Give the extent of all Plasmodium vivax-infected red blood cells.
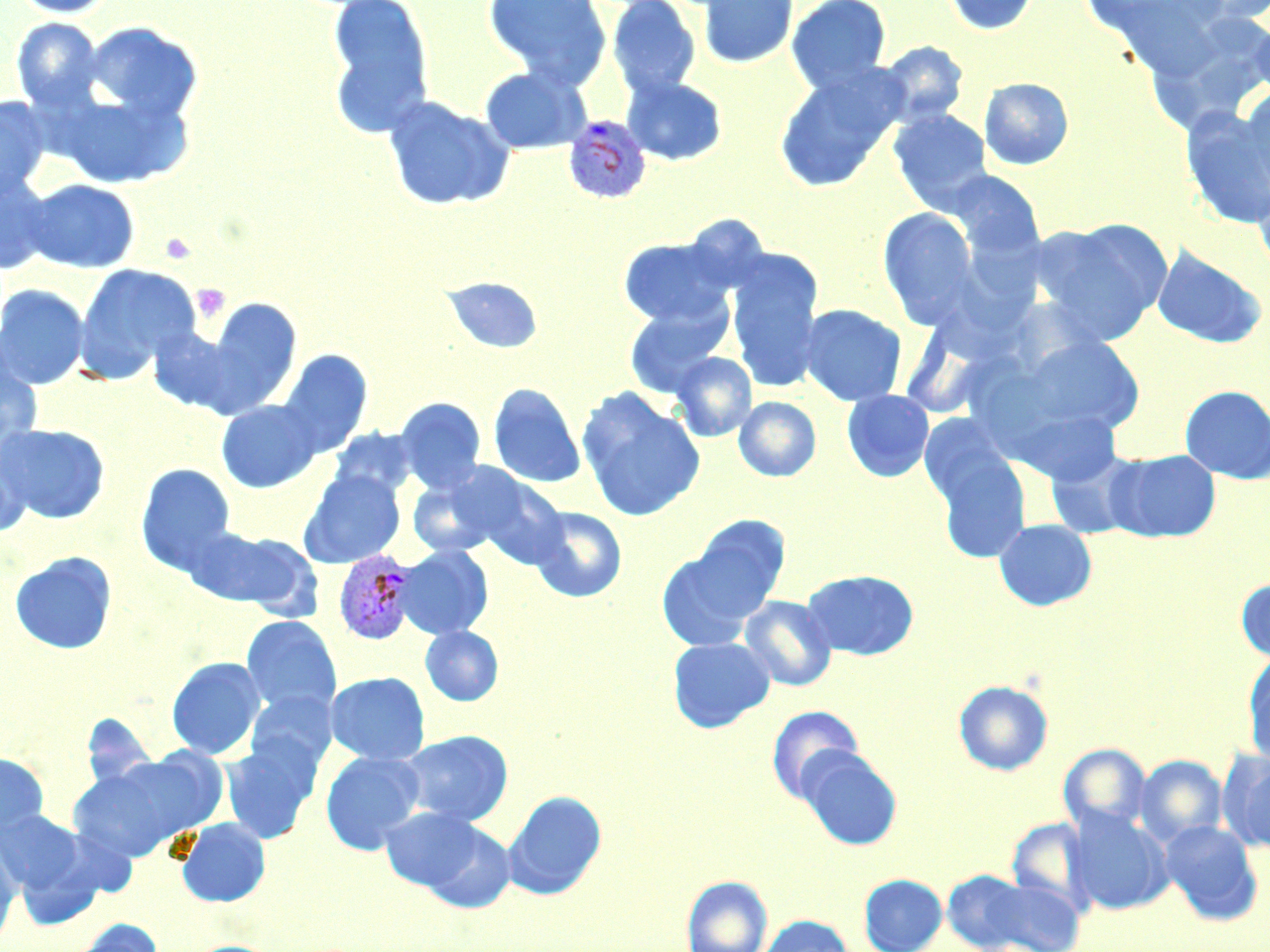
Approximate bounding boxes as named x1/y1/x2/y2 corners in pixels.
Plasmodium vivax-infected red blood cells: (x1=563, y1=115, x2=652, y2=203), (x1=334, y1=550, x2=418, y2=645).

Summary:
  - Uninfected red blood cell locations: (x1=9, y1=0, x2=118, y2=18), (x1=326, y1=0, x2=436, y2=137), (x1=483, y1=0, x2=611, y2=88), (x1=607, y1=0, x2=701, y2=100), (x1=697, y1=0, x2=798, y2=69), (x1=786, y1=0, x2=891, y2=94), (x1=939, y1=0, x2=1040, y2=36), (x1=1188, y1=0, x2=1270, y2=26), (x1=1249, y1=15, x2=1270, y2=100), (x1=11, y1=17, x2=105, y2=112), (x1=83, y1=21, x2=203, y2=122), (x1=878, y1=41, x2=968, y2=128), (x1=774, y1=66, x2=907, y2=192), (x1=480, y1=67, x2=587, y2=154), (x1=622, y1=76, x2=728, y2=166), (x1=979, y1=77, x2=1074, y2=170), (x1=1236, y1=86, x2=1270, y2=197), (x1=51, y1=88, x2=193, y2=189), (x1=0, y1=96, x2=51, y2=200), (x1=383, y1=96, x2=515, y2=211), (x1=1181, y1=108, x2=1270, y2=228), (x1=889, y1=109, x2=992, y2=214), (x1=947, y1=169, x2=1045, y2=262), (x1=0, y1=171, x2=55, y2=274), (x1=23, y1=178, x2=139, y2=273), (x1=1253, y1=178, x2=1270, y2=279), (x1=878, y1=208, x2=979, y2=327), (x1=1031, y1=220, x2=1172, y2=344), (x1=618, y1=237, x2=733, y2=328), (x1=1151, y1=245, x2=1268, y2=349), (x1=726, y1=250, x2=825, y2=393), (x1=73, y1=263, x2=199, y2=382), (x1=443, y1=276, x2=544, y2=354), (x1=0, y1=284, x2=90, y2=389), (x1=201, y1=297, x2=302, y2=410), (x1=623, y1=301, x2=731, y2=399), (x1=799, y1=304, x2=907, y2=406), (x1=146, y1=326, x2=242, y2=414), (x1=1020, y1=335, x2=1145, y2=436), (x1=0, y1=344, x2=44, y2=458), (x1=278, y1=350, x2=373, y2=457), (x1=671, y1=352, x2=757, y2=441), (x1=488, y1=383, x2=586, y2=488), (x1=1179, y1=385, x2=1270, y2=484), (x1=577, y1=389, x2=706, y2=521), (x1=842, y1=390, x2=934, y2=482), (x1=734, y1=396, x2=821, y2=482), (x1=395, y1=397, x2=486, y2=494), (x1=216, y1=400, x2=322, y2=493), (x1=1019, y1=410, x2=1122, y2=487), (x1=918, y1=413, x2=1014, y2=512), (x1=0, y1=423, x2=110, y2=524), (x1=327, y1=426, x2=418, y2=500), (x1=0, y1=444, x2=31, y2=538), (x1=933, y1=446, x2=1032, y2=564), (x1=1045, y1=448, x2=1143, y2=540), (x1=1108, y1=449, x2=1221, y2=543), (x1=136, y1=463, x2=236, y2=576), (x1=300, y1=470, x2=405, y2=568), (x1=406, y1=472, x2=503, y2=558), (x1=471, y1=474, x2=569, y2=569), (x1=528, y1=506, x2=627, y2=603), (x1=678, y1=515, x2=791, y2=627), (x1=994, y1=519, x2=1098, y2=612), (x1=192, y1=527, x2=322, y2=617), (x1=655, y1=543, x2=769, y2=651), (x1=394, y1=545, x2=494, y2=640), (x1=9, y1=551, x2=117, y2=655), (x1=801, y1=569, x2=919, y2=660), (x1=1236, y1=578, x2=1270, y2=663), (x1=739, y1=595, x2=837, y2=691), (x1=241, y1=616, x2=342, y2=717), (x1=420, y1=625, x2=503, y2=706), (x1=667, y1=637, x2=775, y2=733), (x1=1243, y1=653, x2=1270, y2=765), (x1=166, y1=656, x2=266, y2=760), (x1=326, y1=671, x2=430, y2=765), (x1=953, y1=680, x2=1053, y2=775), (x1=246, y1=691, x2=337, y2=773), (x1=767, y1=705, x2=864, y2=803), (x1=399, y1=729, x2=513, y2=827), (x1=221, y1=738, x2=321, y2=844), (x1=1059, y1=743, x2=1151, y2=834), (x1=797, y1=747, x2=903, y2=850), (x1=100, y1=750, x2=229, y2=844), (x1=320, y1=751, x2=425, y2=855), (x1=1220, y1=751, x2=1270, y2=854), (x1=0, y1=753, x2=49, y2=836), (x1=1135, y1=755, x2=1227, y2=846), (x1=66, y1=762, x2=193, y2=862), (x1=503, y1=790, x2=607, y2=899), (x1=380, y1=806, x2=484, y2=892), (x1=0, y1=809, x2=85, y2=896), (x1=1065, y1=809, x2=1173, y2=915), (x1=176, y1=817, x2=271, y2=907), (x1=1006, y1=818, x2=1097, y2=915), (x1=417, y1=819, x2=516, y2=914), (x1=1160, y1=820, x2=1263, y2=925), (x1=0, y1=841, x2=21, y2=944), (x1=859, y1=874, x2=947, y2=952), (x1=963, y1=874, x2=1087, y2=952), (x1=682, y1=876, x2=772, y2=952), (x1=756, y1=915, x2=855, y2=952), (x1=66, y1=919, x2=163, y2=952), (x1=187, y1=940, x2=279, y2=952)
  - Platelet locations: (x1=161, y1=232, x2=197, y2=265), (x1=191, y1=283, x2=231, y2=324)
  - Slide-level diagnosis: Plasmodium vivax
  - Magnification: 1000x
  - Modality: optical microscopy
  - Field of view: single
  - Image size: 1270×952 pixels
  - Preparation: thin blood smear
  - Stain: May-Grünwald-Giemsa